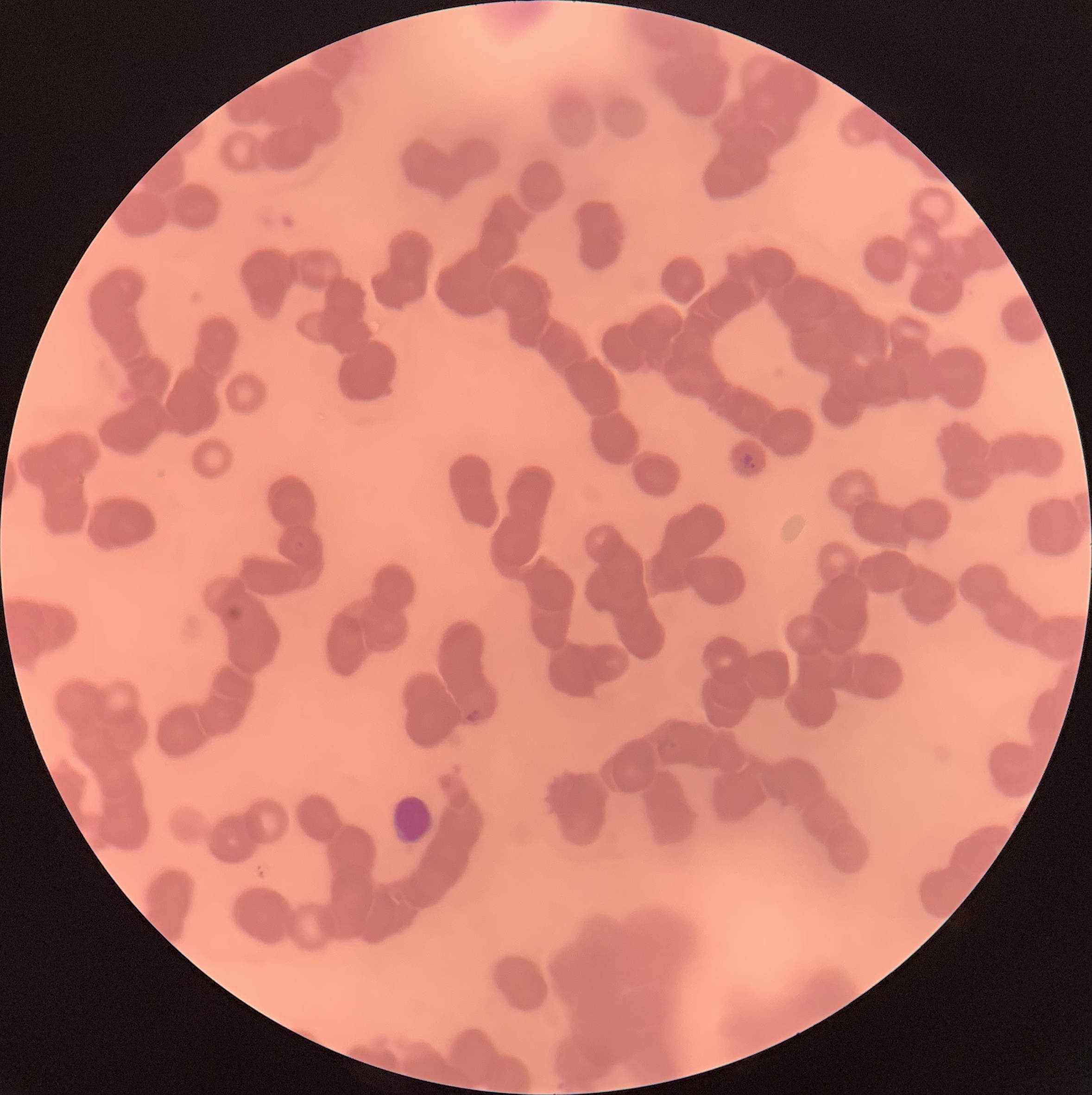

coordinate format = approximate bounding boxes as named x1/y1/x2/y2 corners in pixels
white blood cell locations = (x1=389, y1=794, x2=434, y2=849)
Plasmodium parasite locations = (x1=739, y1=452, x2=756, y2=470), (x1=465, y1=706, x2=482, y2=724)
red blood cell morphology = rouleaux formation
preparation = thin blood film
modality = optical microscopy
image size = 1092×1095 pixels